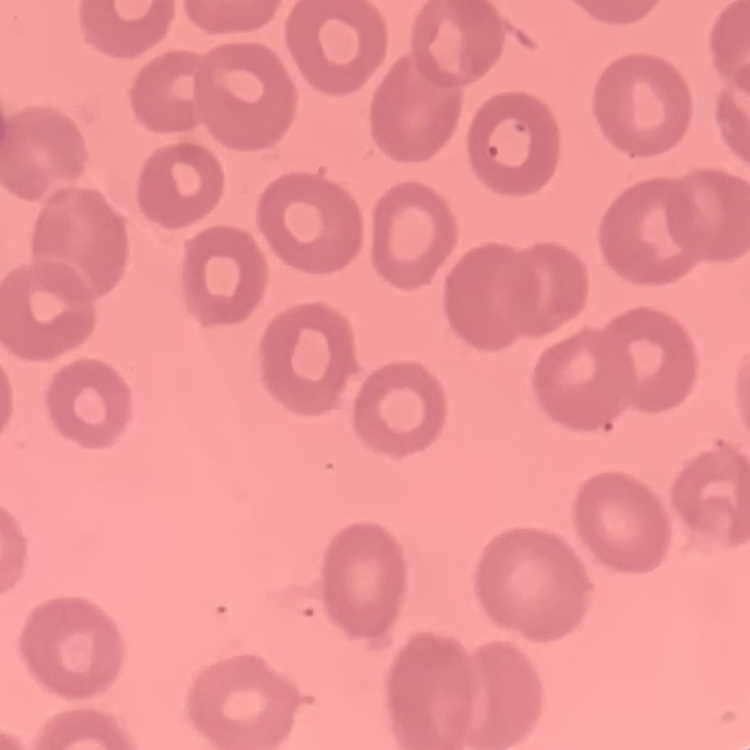 The red blood cells show no rouleaux formation. Stained with either Field's or Giemsa. Square crop of a larger photomicrograph. Thin blood film.